Name the parasite shown.
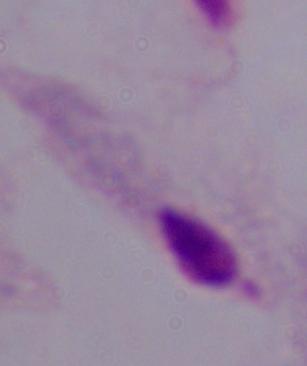
This is a trichomonad.

1000x magnification. Micrograph.